Name the blood parasite species.
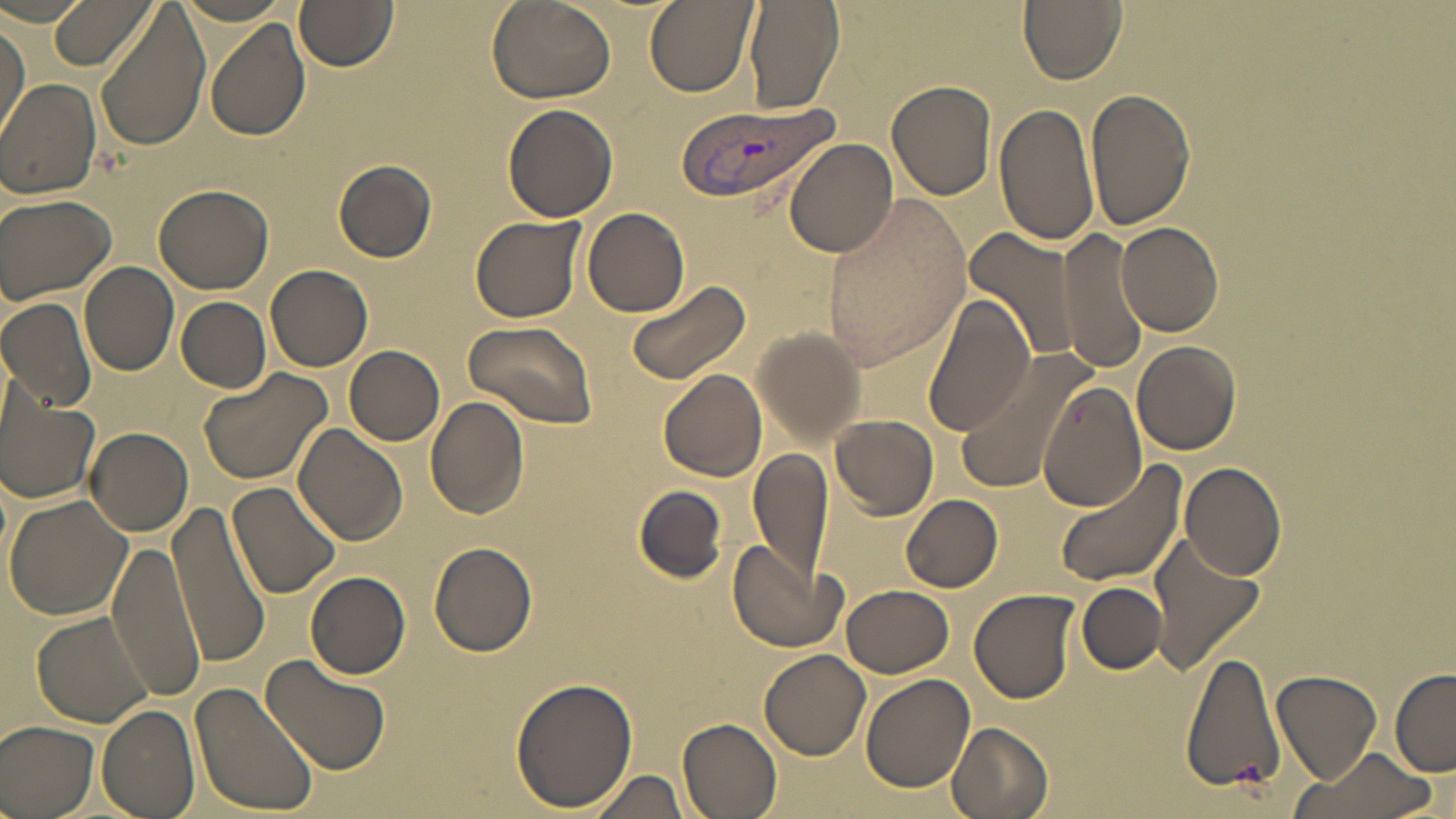
Plasmodium vivax.

Summary:
  - Coordinate format: approximate bounding boxes as named x1/y1/x2/y2 corners in pixels
  - Plasmodium vivax-infected red blood cell locations: (x1=677, y1=98, x2=837, y2=208)
  - Uninfected red blood cell locations: (x1=49, y1=0, x2=156, y2=72), (x1=646, y1=0, x2=755, y2=96), (x1=743, y1=0, x2=844, y2=115), (x1=1018, y1=0, x2=1127, y2=84), (x1=487, y1=1, x2=615, y2=105), (x1=296, y1=2, x2=398, y2=72), (x1=96, y1=9, x2=211, y2=149), (x1=204, y1=19, x2=311, y2=143), (x1=1, y1=21, x2=28, y2=139), (x1=0, y1=78, x2=102, y2=199), (x1=887, y1=80, x2=997, y2=201), (x1=1085, y1=89, x2=1196, y2=231), (x1=994, y1=100, x2=1100, y2=249), (x1=502, y1=103, x2=618, y2=223), (x1=784, y1=138, x2=898, y2=258), (x1=333, y1=160, x2=437, y2=262), (x1=154, y1=182, x2=274, y2=293), (x1=1, y1=193, x2=117, y2=304), (x1=823, y1=194, x2=970, y2=372), (x1=582, y1=208, x2=690, y2=318), (x1=470, y1=214, x2=586, y2=324), (x1=1116, y1=220, x2=1224, y2=337), (x1=965, y1=226, x2=1080, y2=366), (x1=1058, y1=227, x2=1150, y2=375), (x1=80, y1=262, x2=179, y2=375), (x1=265, y1=265, x2=372, y2=370), (x1=621, y1=279, x2=750, y2=385), (x1=921, y1=290, x2=1033, y2=437), (x1=0, y1=296, x2=99, y2=412), (x1=176, y1=297, x2=271, y2=391), (x1=463, y1=321, x2=597, y2=428), (x1=752, y1=326, x2=866, y2=445), (x1=1133, y1=341, x2=1241, y2=454), (x1=345, y1=346, x2=444, y2=445), (x1=956, y1=346, x2=1093, y2=491), (x1=199, y1=365, x2=333, y2=487), (x1=660, y1=368, x2=766, y2=481), (x1=1038, y1=387, x2=1151, y2=510), (x1=1, y1=388, x2=101, y2=506), (x1=425, y1=396, x2=530, y2=518), (x1=831, y1=413, x2=938, y2=518), (x1=296, y1=426, x2=408, y2=548), (x1=84, y1=427, x2=193, y2=535), (x1=749, y1=449, x2=833, y2=583), (x1=1054, y1=461, x2=1189, y2=587), (x1=1179, y1=461, x2=1287, y2=581), (x1=228, y1=480, x2=341, y2=603), (x1=632, y1=486, x2=728, y2=584), (x1=4, y1=494, x2=132, y2=622), (x1=900, y1=494, x2=1003, y2=592), (x1=166, y1=500, x2=274, y2=664), (x1=1150, y1=535, x2=1267, y2=675), (x1=107, y1=538, x2=205, y2=699), (x1=728, y1=538, x2=847, y2=653), (x1=428, y1=542, x2=537, y2=657), (x1=305, y1=571, x2=410, y2=679), (x1=1078, y1=582, x2=1166, y2=674), (x1=842, y1=585, x2=955, y2=678), (x1=969, y1=589, x2=1080, y2=704), (x1=31, y1=610, x2=156, y2=729), (x1=1180, y1=647, x2=1286, y2=797), (x1=759, y1=650, x2=869, y2=760), (x1=260, y1=653, x2=391, y2=776), (x1=1390, y1=668, x2=1456, y2=775), (x1=1272, y1=670, x2=1383, y2=785), (x1=860, y1=671, x2=975, y2=793), (x1=509, y1=677, x2=638, y2=811), (x1=189, y1=681, x2=317, y2=815), (x1=98, y1=705, x2=199, y2=819), (x1=678, y1=717, x2=783, y2=819), (x1=0, y1=720, x2=100, y2=819), (x1=947, y1=722, x2=1055, y2=819), (x1=1292, y1=749, x2=1436, y2=819), (x1=586, y1=768, x2=689, y2=818)
  - Preparation: thin blood smear
  - Field of view: one of a larger specimen
  - Image size: 1456×819 pixels
  - Stain: May-Grünwald-Giemsa
  - Magnification: 1000x
  - Modality: optical microscopy